Outline each blood parasite and name the species.
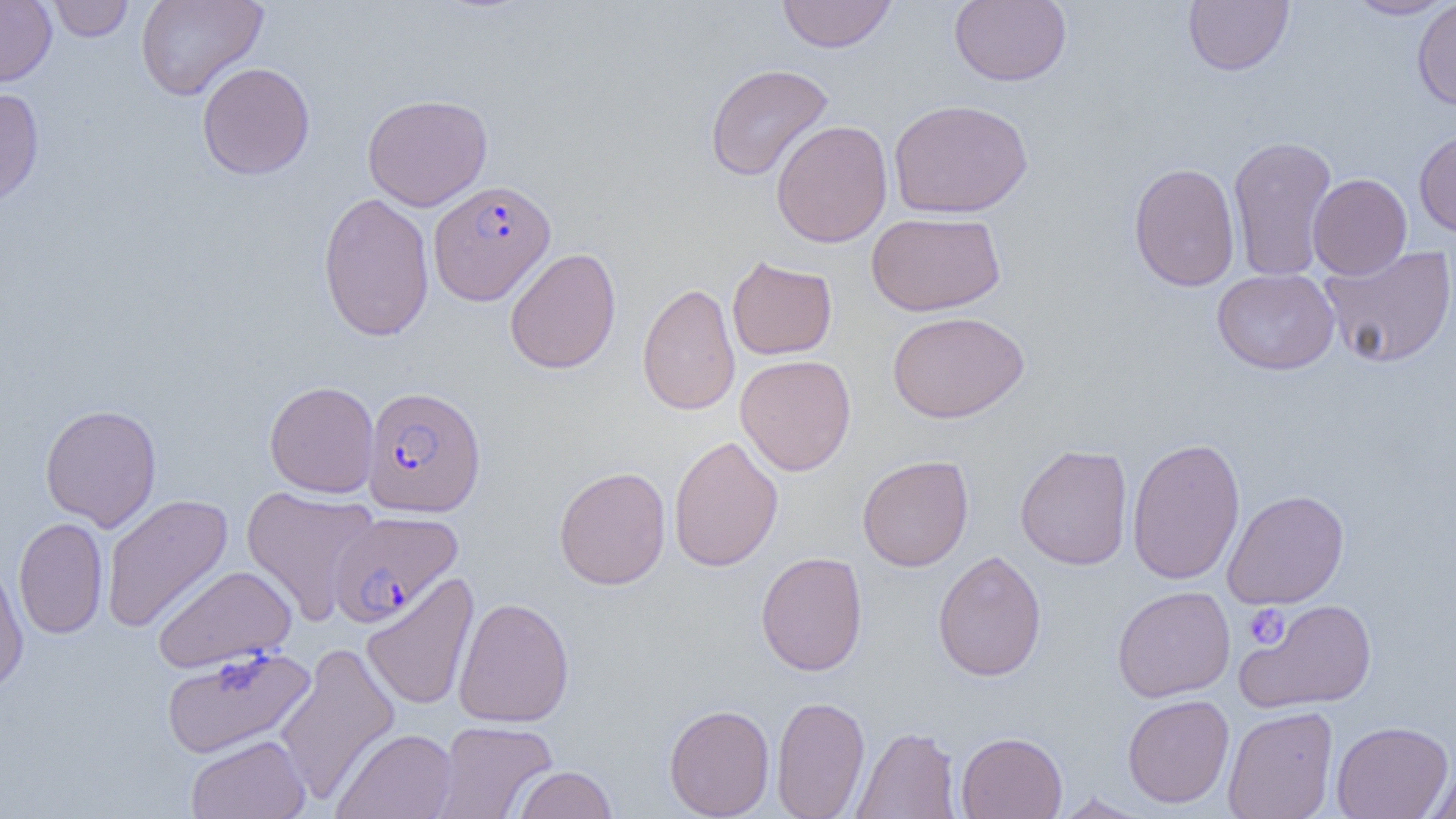

Approximate bounding boxes as (x1, y1, x2, y2) in pixels.
Plasmodium falciparum-infected red blood cells: (429, 180, 556, 305), (362, 386, 486, 518), (329, 511, 463, 626).
No Plasmodium ovale, Plasmodium malariae, Plasmodium vivax, Babesia divergens, or Trypanosoma brucei observed.

Uninfected red blood cell locations: (0, 0, 57, 86), (47, 0, 134, 42), (136, 0, 268, 101), (776, 0, 897, 52), (949, 0, 1072, 86), (1183, 0, 1294, 76), (1343, 0, 1454, 20), (1412, 0, 1456, 110), (197, 61, 315, 180), (703, 63, 834, 182), (0, 86, 44, 210), (362, 93, 493, 211), (888, 98, 1033, 218), (770, 120, 892, 247), (1414, 127, 1456, 238), (1227, 134, 1338, 283), (1129, 162, 1241, 291), (1308, 173, 1412, 280), (318, 191, 435, 342), (866, 212, 1006, 316), (1319, 245, 1456, 368), (504, 247, 621, 374), (726, 255, 838, 360), (1212, 268, 1339, 375), (637, 281, 740, 416), (888, 310, 1029, 423), (735, 354, 856, 476), (264, 380, 380, 498), (39, 403, 162, 532), (668, 435, 783, 573), (1127, 437, 1246, 585), (1014, 443, 1133, 570), (857, 454, 974, 571), (554, 466, 671, 590), (240, 485, 379, 625), (1222, 489, 1349, 609), (101, 493, 233, 633), (14, 516, 108, 639), (755, 551, 868, 676), (932, 551, 1047, 682), (0, 560, 29, 694), (152, 565, 298, 672), (361, 573, 479, 712), (1112, 586, 1235, 702), (453, 596, 575, 728), (1236, 599, 1378, 712), (274, 641, 400, 806), (160, 646, 315, 759), (1122, 694, 1234, 809), (771, 695, 870, 819), (663, 704, 775, 818), (1223, 706, 1339, 819), (429, 720, 557, 818), (1331, 720, 1453, 818), (851, 726, 961, 818), (331, 728, 458, 819), (955, 731, 1067, 819), (185, 734, 311, 819), (1425, 760, 1456, 819), (512, 765, 617, 818), (1052, 792, 1152, 818). Platelet locations: (1243, 604, 1290, 649). Slide-level diagnosis: Plasmodium falciparum. 1000x magnification. Optical microscopy. One field of a larger specimen. Image is 1456×819 pixels. Thin blood film.